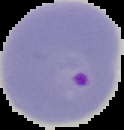

Summary:
  - Image type: segmented cell region with the area outside set to black
  - Image size: 124×130 pixels
  - Preparation: thin blood film
  - Result: Plasmodium parasites detected